Classify this cell by malaria status.
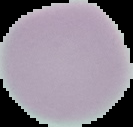

It is uninfected.

Image is 133×127 pixels. The area outside the segmented cell region is set to black. From a thin blood smear.